Locate every malaria parasite and every leukocyte.
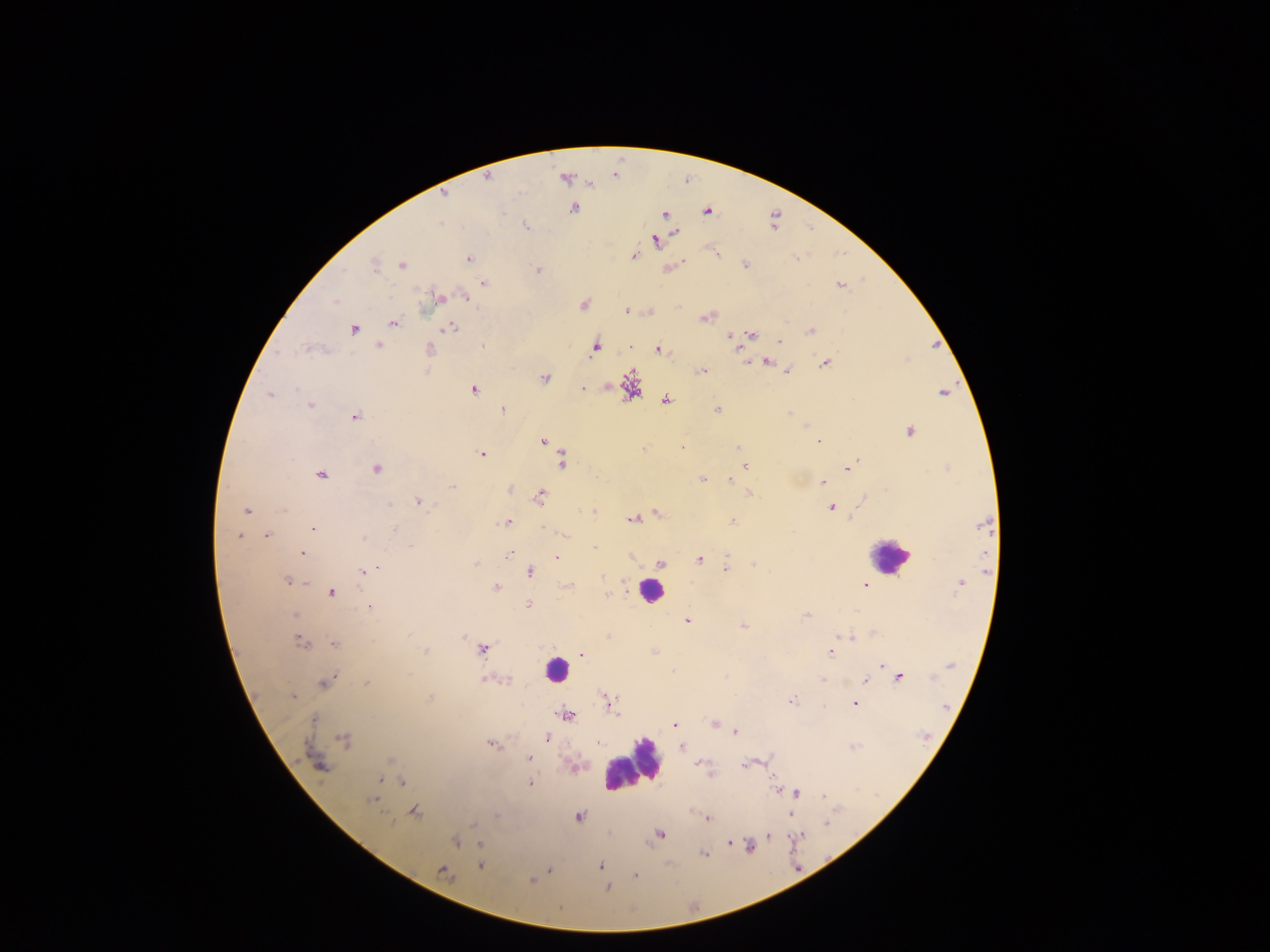

Approximate centers as x y in pixels.
Malaria parasites: 592 184; 444 194; 573 208; 707 212; 664 214; 440 224; 527 225; 676 232; 655 240; 633 256; 468 258; 402 264; 374 265; 745 265; 538 270; 483 283; 840 285; 438 296; 465 297; 334 301; 583 305; 628 311; 704 317; 393 323; 353 328; 451 328; 811 331; 751 334; 729 336; 780 341; 378 344; 482 346; 306 348; 595 348; 429 350; 658 350; 767 362; 825 363; 787 370; 701 371; 544 379; 630 386; 582 388; 296 389; 473 390; 943 392; 269 394; 665 399; 310 405; 503 409; 717 410; 788 414; 355 416; 806 426; 909 432; 543 442; 820 442; 683 447; 738 447; 643 449; 481 454; 561 461; 745 466; 377 468; 848 468; 320 475; 703 479; 730 480; 822 482; 453 487; 510 489; 749 494; 540 496; 418 501; 390 505; 831 508; 284 510; 247 511; 593 511; 657 513; 633 519; 506 522; 733 522; 982 524; 313 528; 394 529; 544 529; 564 534; 239 536; 267 536; 363 539; 409 546; 594 547; 302 553; 509 554; 727 556; 557 558; 699 560; 660 563; 475 564; 754 565; 378 568; 726 569; 362 572; 530 572; 603 577; 287 581; 305 582; 960 584; 864 585; 496 587; 568 587; 331 592; 608 594; 528 604; 369 607; 295 615; 807 616; 687 621; 743 625; 463 636; 850 637; 300 642; 334 644; 483 649; 425 651; 655 652; 831 652; 582 654; 882 665; 409 673; 899 677; 822 679; 483 680; 507 680; 866 680; 325 682; 366 684; 293 697; 430 698; 792 701; 854 703; 611 705; 824 707; 567 715; 713 723; 675 725; 736 731; 547 739; 343 740; 598 743; 490 744; 681 747; 529 758; 391 760; 753 762; 703 765; 746 765; 320 767; 709 771; 379 781; 402 782; 530 783; 777 788; 797 793; 824 796; 373 799; 414 812; 790 813; 497 816; 579 817; 707 818; 828 823; 472 825; 660 834; 769 836; 800 836; 454 841; 729 843; 480 844; 749 846; 704 854; 480 865; 601 866; 549 869; 441 871; 635 875; 532 880; 606 888.
Leukocytes: 890 556; 650 591; 555 671; 632 765.

Summary:
  - Capture: mobile-phone photograph through a microscope
  - Image size: 1270×952 pixels
  - Country: Ghana
  - Field of view: single
  - Preparation: thick blood smear